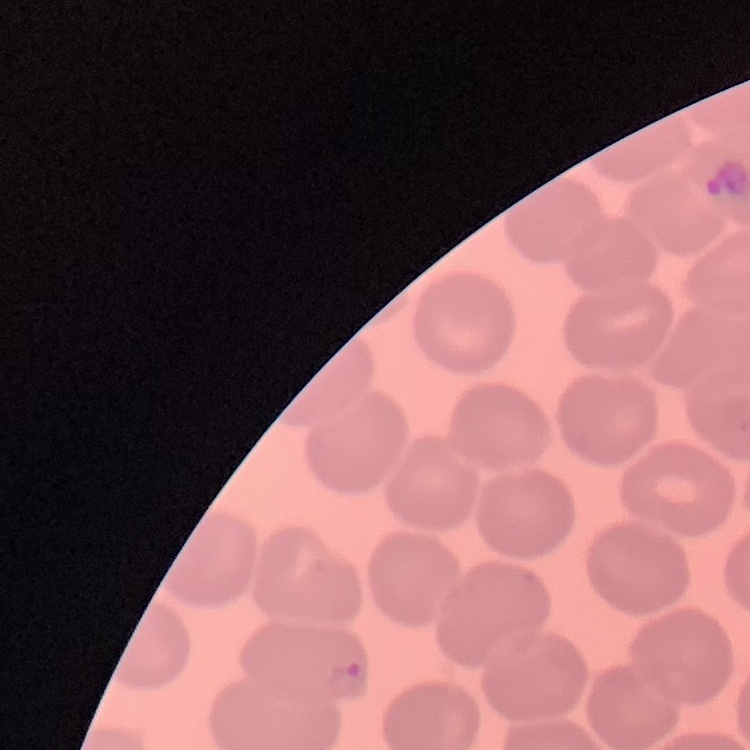
Summary:
  - Red blood cell morphology: no rouleaux formation
  - Stain: Field's or Giemsa
  - Image type: square crop of a larger photomicrograph
  - Preparation: thin blood film